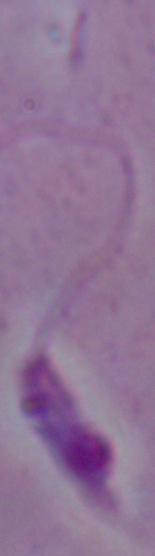
{
  "modality": "micrograph",
  "identification": "Leishmania",
  "magnification": "1000x"
}